Point out each Plasmodium parasite.
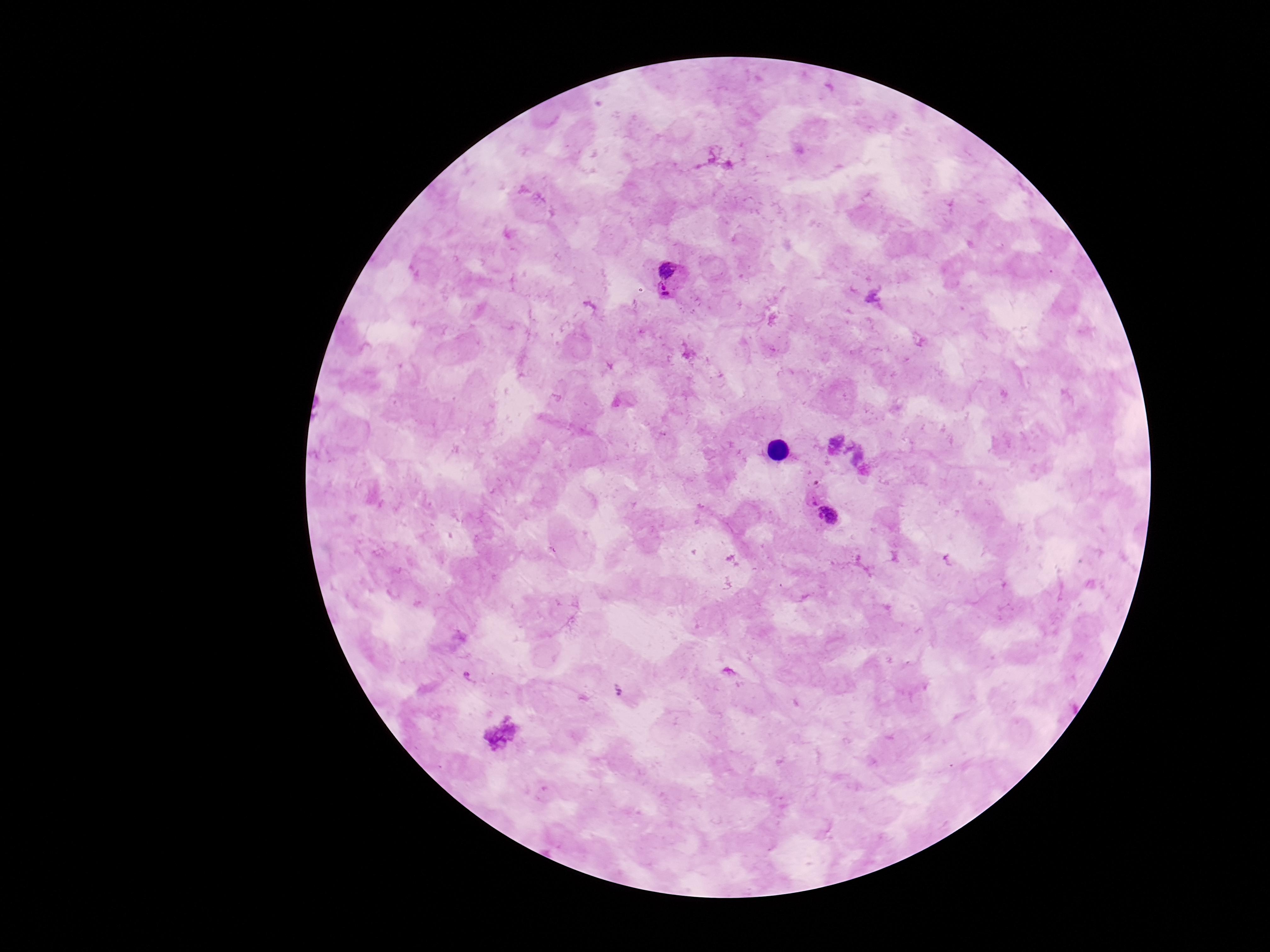
Approximate centers as (x, y) in pixels.
Plasmodium parasites: (671, 280), (815, 487), (828, 515).

image size = 1270×952 pixels
capture = smartphone camera through the microscope eyepiece
preparation = thick blood film
magnification = 100x
patient malaria status = positive
stain = Giemsa
field of view = single